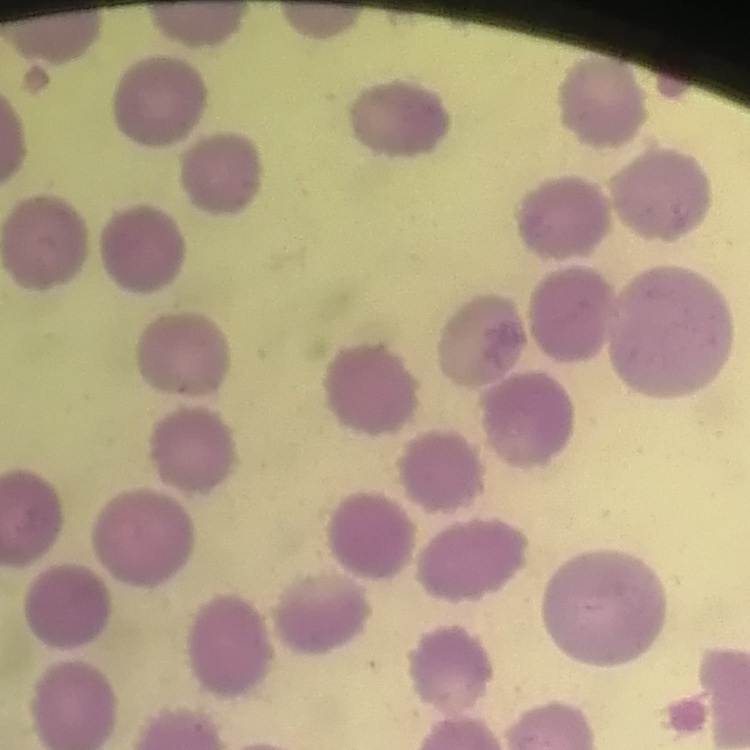

erythrocyte morphology = no rouleaux formation
image type = one tile cut from a larger photomicrograph
stain = Field's or Giemsa
preparation = thin blood smear